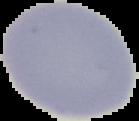

Summary:
  - Image type: cell region segmented out of the field of view; surrounding area masked to black
  - Preparation: thin blood film
  - Image size: 139×121 pixels
  - Malaria status: uninfected